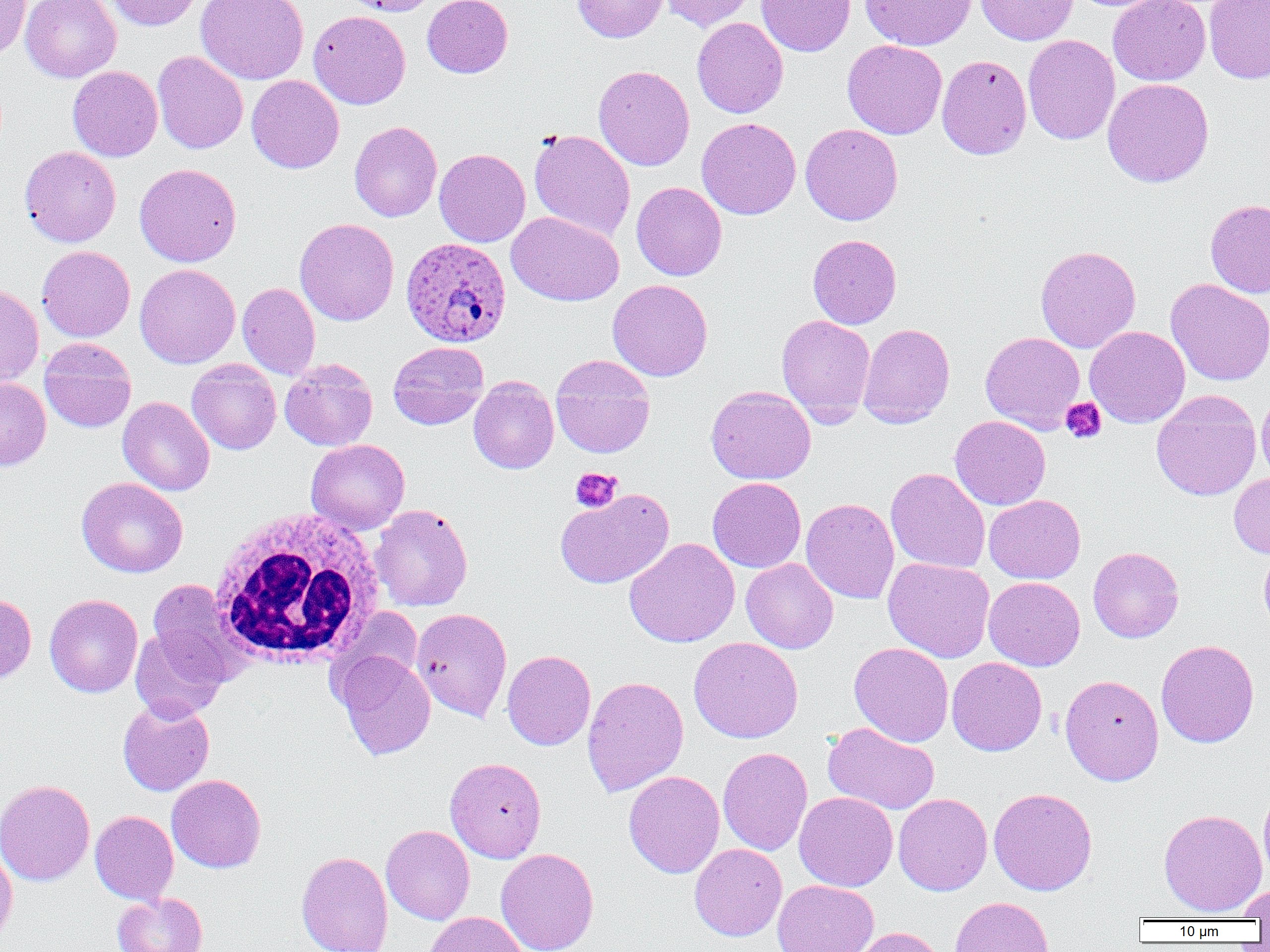

Approximate bounding boxes as named x1/y1/x2/y2 corners in pixels. White blood cell locations: (x1=207, y1=507, x2=386, y2=669). Plasmodium ovale-infected red blood cell locations: (x1=401, y1=237, x2=511, y2=347). Platelet locations: (x1=1060, y1=397, x2=1106, y2=444), (x1=570, y1=467, x2=623, y2=513). Uninfected red blood cell locations: (x1=21, y1=0, x2=121, y2=82), (x1=104, y1=0, x2=201, y2=30), (x1=196, y1=0, x2=309, y2=84), (x1=342, y1=0, x2=438, y2=16), (x1=422, y1=0, x2=513, y2=78), (x1=572, y1=0, x2=669, y2=42), (x1=661, y1=0, x2=756, y2=31), (x1=757, y1=0, x2=855, y2=56), (x1=860, y1=0, x2=977, y2=51), (x1=975, y1=0, x2=1078, y2=45), (x1=1108, y1=0, x2=1210, y2=86), (x1=1204, y1=0, x2=1270, y2=83), (x1=0, y1=1, x2=31, y2=58), (x1=310, y1=7, x2=513, y2=93), (x1=309, y1=10, x2=410, y2=109), (x1=692, y1=17, x2=788, y2=118), (x1=1023, y1=35, x2=1120, y2=144), (x1=842, y1=39, x2=947, y2=139), (x1=152, y1=50, x2=248, y2=154), (x1=937, y1=54, x2=1031, y2=159), (x1=593, y1=65, x2=694, y2=171), (x1=68, y1=66, x2=162, y2=161), (x1=247, y1=75, x2=344, y2=173), (x1=1102, y1=78, x2=1214, y2=188), (x1=696, y1=117, x2=801, y2=219), (x1=349, y1=121, x2=442, y2=222), (x1=800, y1=123, x2=903, y2=225), (x1=529, y1=129, x2=635, y2=242), (x1=20, y1=145, x2=121, y2=247), (x1=434, y1=148, x2=530, y2=247), (x1=134, y1=163, x2=242, y2=267), (x1=631, y1=181, x2=727, y2=281), (x1=1205, y1=199, x2=1270, y2=298), (x1=506, y1=211, x2=624, y2=306), (x1=294, y1=218, x2=399, y2=326), (x1=808, y1=234, x2=901, y2=329), (x1=1035, y1=245, x2=1141, y2=353), (x1=37, y1=246, x2=136, y2=342), (x1=135, y1=264, x2=241, y2=369), (x1=607, y1=279, x2=713, y2=381), (x1=1165, y1=279, x2=1270, y2=387), (x1=237, y1=282, x2=320, y2=380), (x1=0, y1=283, x2=44, y2=386), (x1=776, y1=315, x2=876, y2=425), (x1=858, y1=323, x2=955, y2=428), (x1=1085, y1=326, x2=1190, y2=427), (x1=980, y1=331, x2=1086, y2=433), (x1=39, y1=338, x2=137, y2=433), (x1=388, y1=341, x2=489, y2=429), (x1=551, y1=356, x2=655, y2=458), (x1=187, y1=359, x2=281, y2=454), (x1=279, y1=359, x2=378, y2=451), (x1=469, y1=376, x2=559, y2=474), (x1=0, y1=377, x2=51, y2=471), (x1=706, y1=385, x2=816, y2=484), (x1=1151, y1=390, x2=1262, y2=501), (x1=1256, y1=392, x2=1270, y2=486), (x1=117, y1=396, x2=215, y2=496), (x1=949, y1=415, x2=1051, y2=510), (x1=306, y1=439, x2=410, y2=535), (x1=885, y1=468, x2=990, y2=574), (x1=1229, y1=472, x2=1270, y2=558), (x1=76, y1=477, x2=188, y2=578), (x1=707, y1=477, x2=806, y2=573), (x1=555, y1=488, x2=674, y2=588), (x1=984, y1=494, x2=1085, y2=584), (x1=801, y1=497, x2=899, y2=604), (x1=370, y1=504, x2=473, y2=611), (x1=624, y1=538, x2=740, y2=648), (x1=1088, y1=547, x2=1184, y2=643), (x1=1258, y1=548, x2=1270, y2=634), (x1=883, y1=557, x2=995, y2=662), (x1=741, y1=558, x2=838, y2=653), (x1=983, y1=576, x2=1085, y2=671), (x1=147, y1=579, x2=245, y2=683), (x1=0, y1=593, x2=36, y2=684), (x1=44, y1=594, x2=143, y2=697), (x1=412, y1=607, x2=512, y2=723), (x1=130, y1=628, x2=228, y2=723), (x1=688, y1=637, x2=803, y2=743), (x1=1156, y1=639, x2=1259, y2=748), (x1=849, y1=642, x2=954, y2=747), (x1=334, y1=650, x2=436, y2=760), (x1=502, y1=650, x2=596, y2=750), (x1=947, y1=657, x2=1047, y2=756), (x1=1060, y1=674, x2=1164, y2=785), (x1=582, y1=675, x2=688, y2=796), (x1=117, y1=698, x2=215, y2=796), (x1=823, y1=722, x2=939, y2=815), (x1=718, y1=747, x2=813, y2=855), (x1=445, y1=757, x2=547, y2=863), (x1=623, y1=770, x2=724, y2=878), (x1=166, y1=774, x2=266, y2=873), (x1=0, y1=779, x2=95, y2=886), (x1=1258, y1=782, x2=1270, y2=887), (x1=988, y1=787, x2=1097, y2=896), (x1=794, y1=791, x2=897, y2=891), (x1=893, y1=793, x2=993, y2=895), (x1=1159, y1=808, x2=1267, y2=916), (x1=90, y1=810, x2=178, y2=905), (x1=381, y1=824, x2=475, y2=925), (x1=689, y1=843, x2=787, y2=941), (x1=0, y1=846, x2=18, y2=947), (x1=496, y1=848, x2=599, y2=952), (x1=296, y1=851, x2=393, y2=952), (x1=772, y1=879, x2=879, y2=952), (x1=1236, y1=883, x2=1270, y2=920), (x1=112, y1=892, x2=207, y2=952), (x1=949, y1=896, x2=1054, y2=952), (x1=424, y1=912, x2=529, y2=952), (x1=847, y1=926, x2=947, y2=952). Slide-level diagnosis: Plasmodium ovale. Single field of view. Optical microscopy. Captured at 1000x magnification. Image is 1270×952 pixels. Thin blood film.